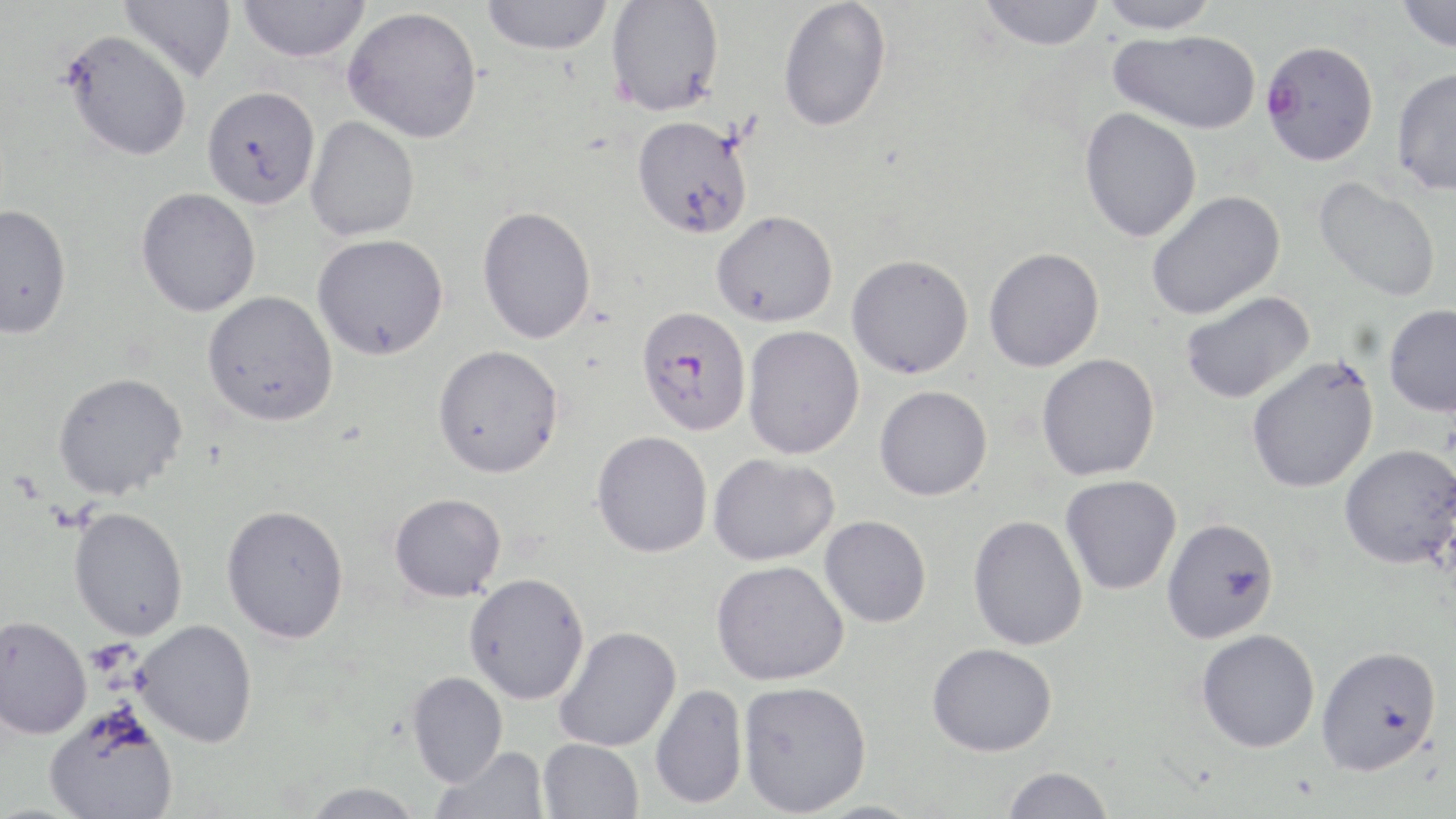
Summary:
  - Coordinate format: approximate bounding boxes as (x1,y1)-(x2,y2) corner pairs in pixels
  - Plasmodium falciparum-infected red blood cell locations: (1260,40)-(1379,165), (637,305)-(752,436)
  - Platelet locations: (8,473)-(42,504)
  - Uninfected red blood cell locations: (119,0)-(236,84), (237,0)-(372,63), (481,0)-(614,55), (778,0)-(891,132), (978,0)-(1106,51), (1096,0)-(1222,34), (1396,0)-(1456,53), (605,1)-(725,116), (343,6)-(483,143), (61,29)-(192,162), (1108,29)-(1261,134), (1391,65)-(1456,196), (201,86)-(320,210), (1079,107)-(1202,242), (631,115)-(754,239), (305,116)-(420,241), (1312,177)-(1442,303), (136,187)-(261,317), (1146,190)-(1285,320), (0,203)-(72,339), (477,206)-(597,344), (712,210)-(838,327), (312,233)-(448,360), (983,247)-(1104,372), (846,254)-(974,379), (202,290)-(338,426), (1180,291)-(1314,404), (1384,304)-(1456,417), (742,325)-(865,459), (433,344)-(564,478), (1036,353)-(1160,481), (1245,354)-(1379,494), (53,372)-(187,500), (874,385)-(992,501), (591,430)-(713,558), (1339,444)-(1456,568), (708,453)-(839,566), (1060,475)-(1182,595), (389,492)-(507,602), (221,503)-(349,643), (69,506)-(188,641), (968,514)-(1088,650), (819,515)-(932,628), (1161,517)-(1280,643), (711,560)-(849,685), (464,572)-(590,704), (0,615)-(92,739), (133,620)-(258,747), (554,625)-(681,752), (1196,628)-(1320,752), (927,643)-(1057,757), (1315,645)-(1442,776), (407,671)-(508,787), (737,680)-(872,816), (649,684)-(748,810), (44,705)-(179,819), (538,738)-(643,819), (432,746)-(549,819), (1001,766)-(1114,819), (301,782)-(426,819)
  - Slide-level diagnosis: Plasmodium falciparum
  - Stain: May-Grünwald-Giemsa
  - Magnification: 1000x
  - Preparation: thin blood smear
  - Field of view: one of a larger specimen
  - Image size: 1456×819 pixels
  - Modality: light microscopy